Give the position of every malaria parasite.
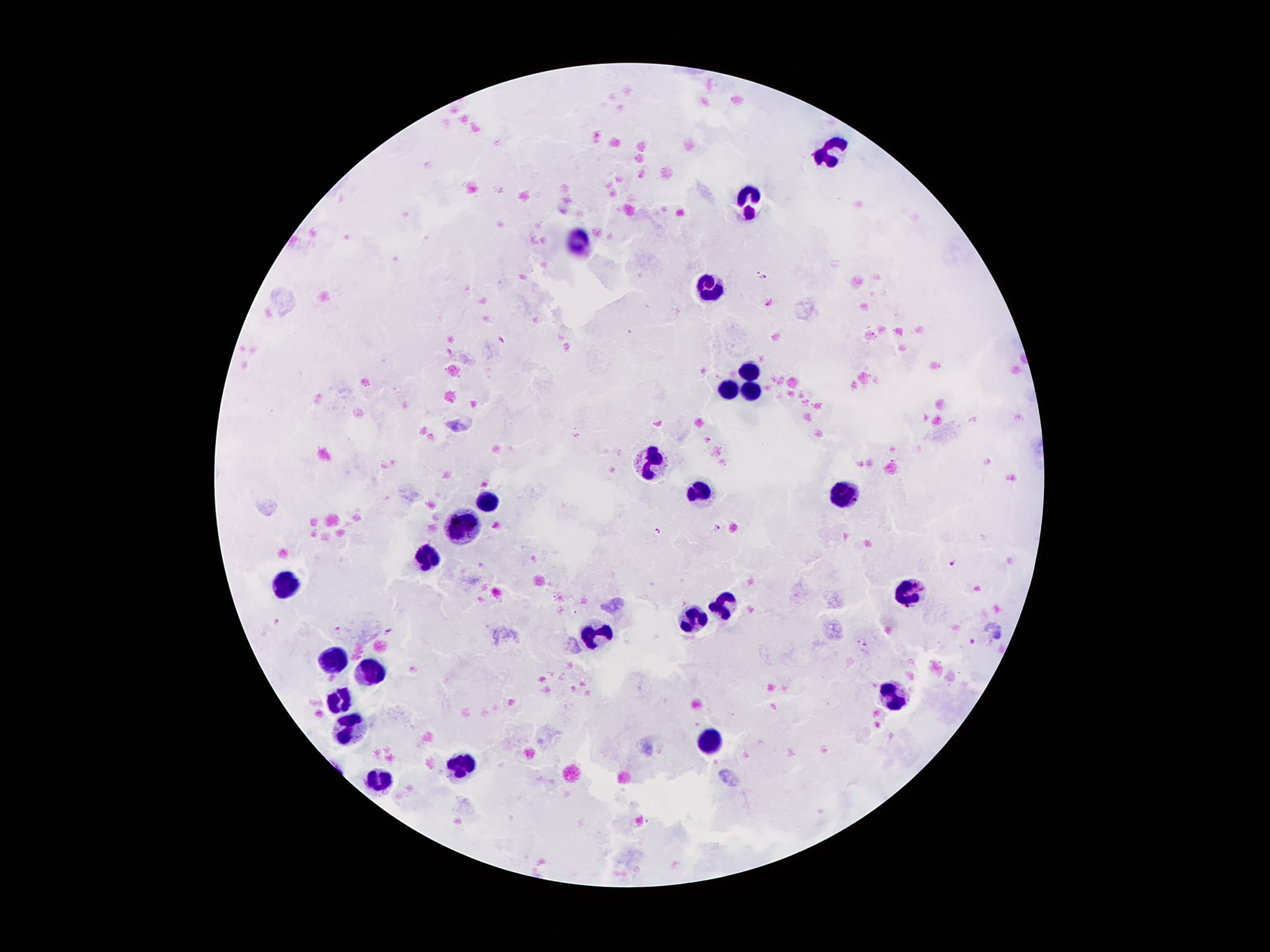

Approximate centers as [x, y] in pixels.
Malaria parasites: [758, 272], [764, 278], [717, 527], [658, 532], [954, 564], [276, 622], [337, 628], [388, 629], [973, 642], [861, 644].

Summary:
  - Leukocyte locations: [831, 152], [747, 200], [580, 245], [710, 290], [747, 371], [748, 386], [725, 391], [653, 460], [701, 494], [844, 495], [488, 504], [466, 531], [429, 557], [286, 583], [910, 591], [726, 605], [691, 620], [596, 632], [332, 660], [372, 673], [891, 698], [341, 703], [349, 731], [709, 742], [461, 765], [378, 783]
  - Field of view: single
  - Capture: smartphone camera through the microscope eyepiece
  - Image size: 1270×952 pixels
  - Patient malaria status: infected with Plasmodium falciparum
  - Stain: Giemsa
  - Preparation: thick peripheral-blood smear
  - Magnification: 100x